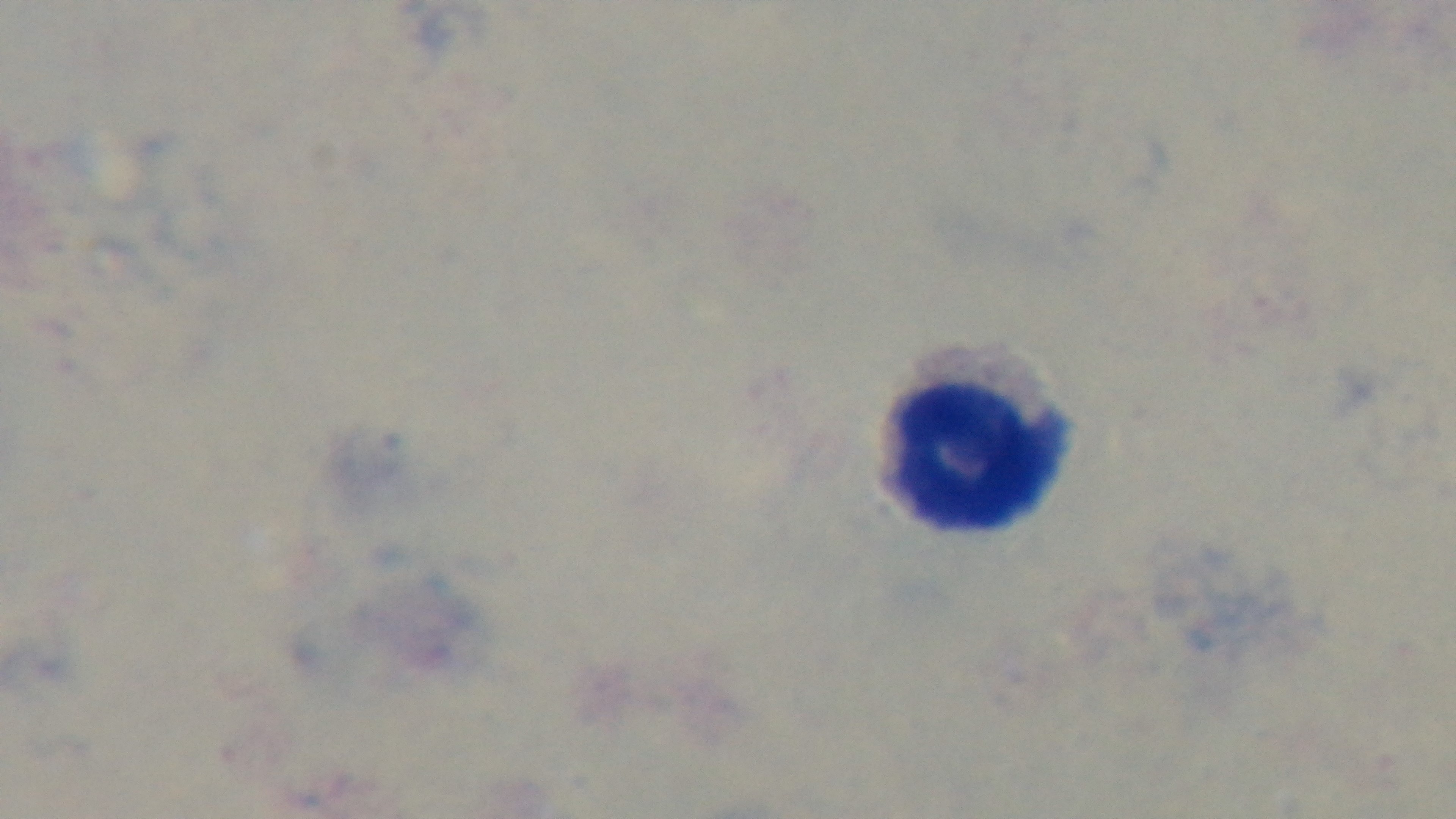
Light microscopy. Giemsa stain. Oil-immersion objective, 100x. One field from the slide. Preparation: thick. Malaria status: uninfected. Mounted 4K digital camera.